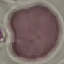
Summary:
  - Result: no malaria parasites detected
  - Stain: Giemsa
  - Preparation: thin blood film
  - Image type: automatically extracted cell patch, resized to 64 × 64 pixels
  - Capture: smartphone camera at the microscope eyepiece